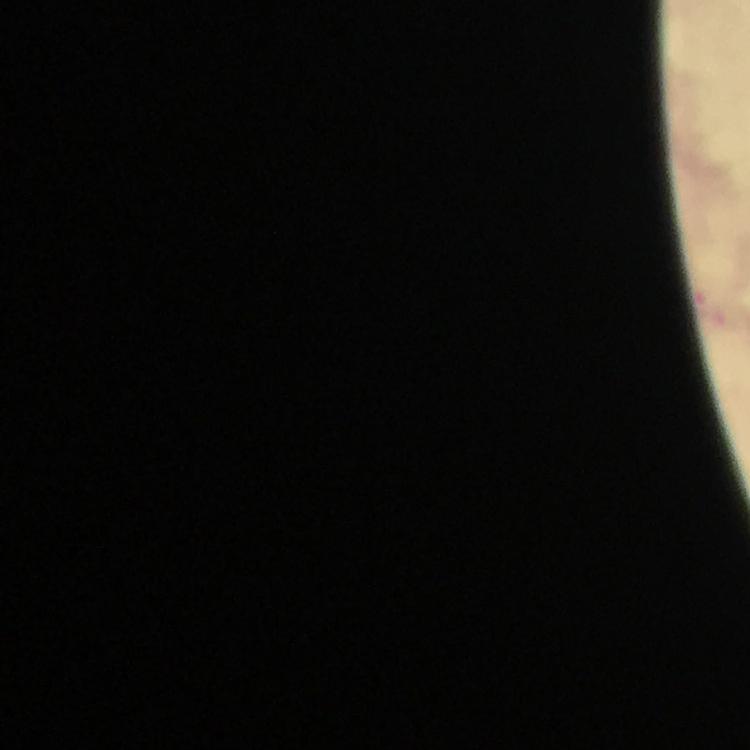

magnification = 100x
capture = smartphone mounted on the microscope
stain = Giemsa
context = from a malaria diagnostic workup
malaria parasite locations = approximate centers as [x, y] in pixels: [707, 308]
image size = 750×750 pixels
cropped from = one field of view
immersion oil = applied
preparation = thick blood film